Classify this cell by malaria status.
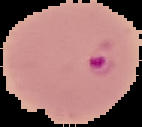
Parasitized.

{
  "preparation": "thin blood film",
  "image_type": "segmented cell region on a black background",
  "image_size": "142×127 pixels"
}